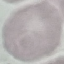
{
  "malaria_status": "uninfected",
  "stain": "Giemsa",
  "capture": "smartphone camera at the microscope eyepiece",
  "image_type": "cell patch, automatically extracted from a larger field of view and resized to 64 × 64 pixels",
  "preparation": "thin smear"
}